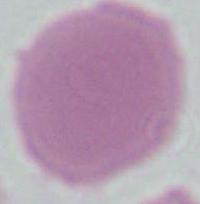
Summary:
  - Identification: erythrocyte
  - Modality: micrograph
  - Magnification: 1000x